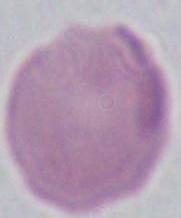

Summary:
  - Modality: micrograph
  - Identification: erythrocyte
  - Magnification: 1000x